Comment on the morphology of the erythrocytes.
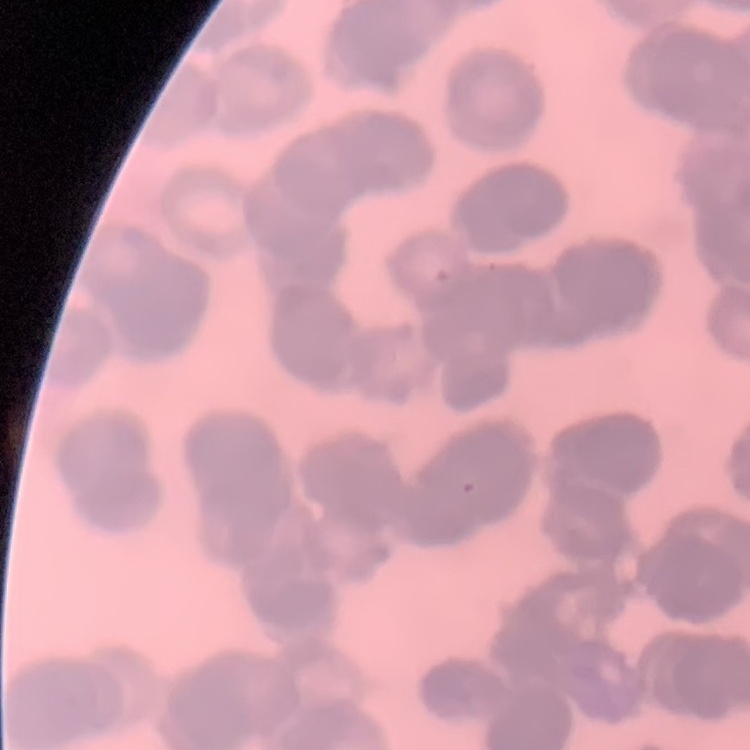

Rouleaux formation.

Field's or Giemsa stain. Thin blood smear. One tile cut from a larger photomicrograph.